Describe the morphology of the erythrocytes.
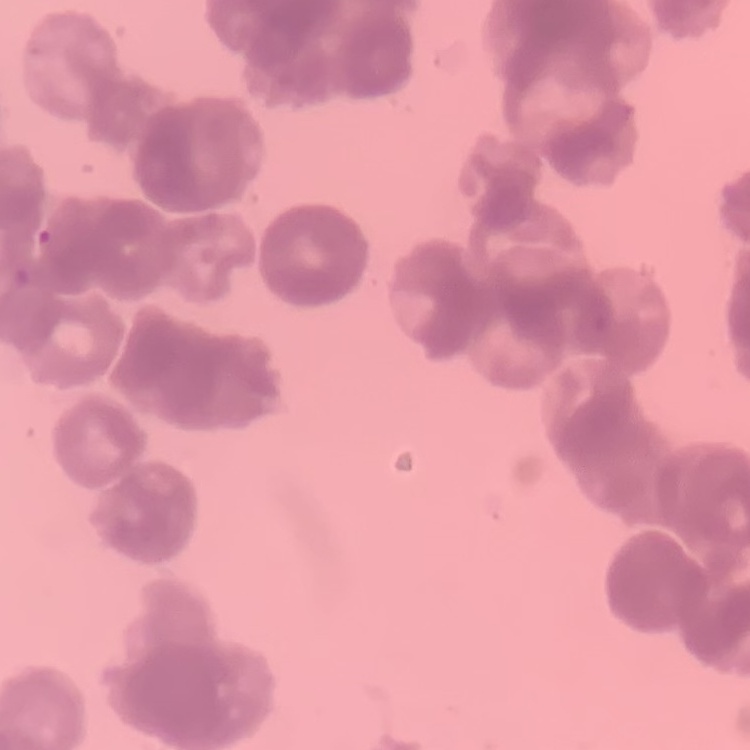

Rouleaux formation.

Thin peripheral smear. Field's or Giemsa stain. One tile cut from a larger photomicrograph.